Describe the morphology of the erythrocytes.
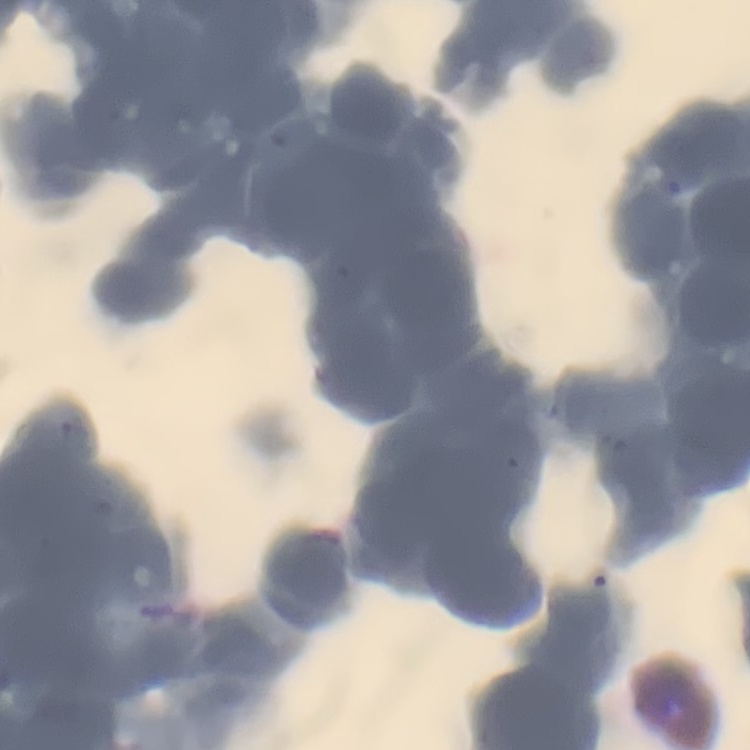
They show rouleaux formation.

{
  "preparation": "thin blood film",
  "stain": "Field's or Giemsa",
  "image_type": "square crop of a larger photomicrograph"
}